Report the malaria status of this cell.
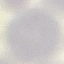

It is uninfected.

Summary:
  - Image type: automatically extracted cell patch, resized to 64 × 64 pixels
  - Stain: Giemsa
  - Preparation: thin blood film
  - Capture: smartphone camera at the microscope eyepiece